Assess the morphology of the red blood cells.
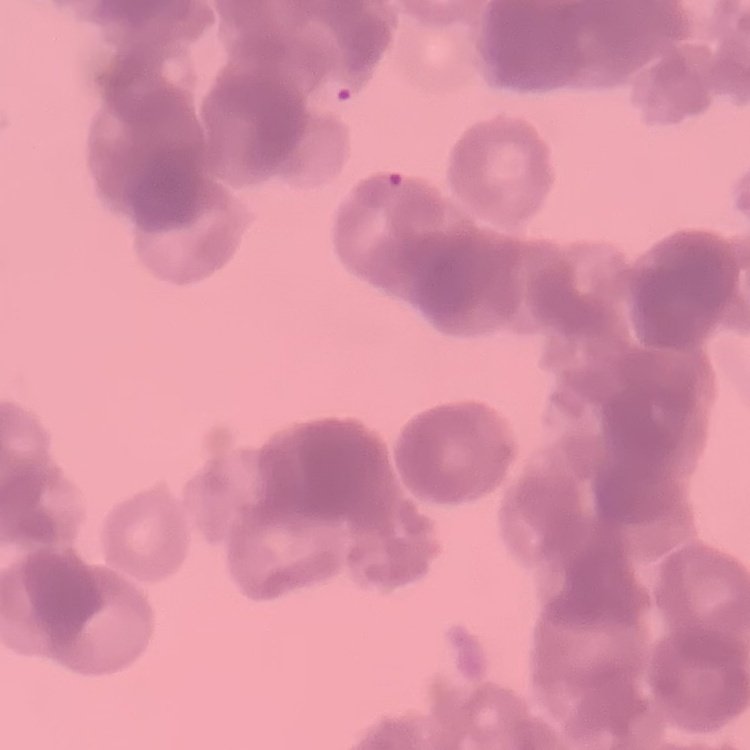
Rouleaux formation.

image type = one tile cut from a larger photomicrograph
preparation = thin blood smear
stain = Field's or Giemsa